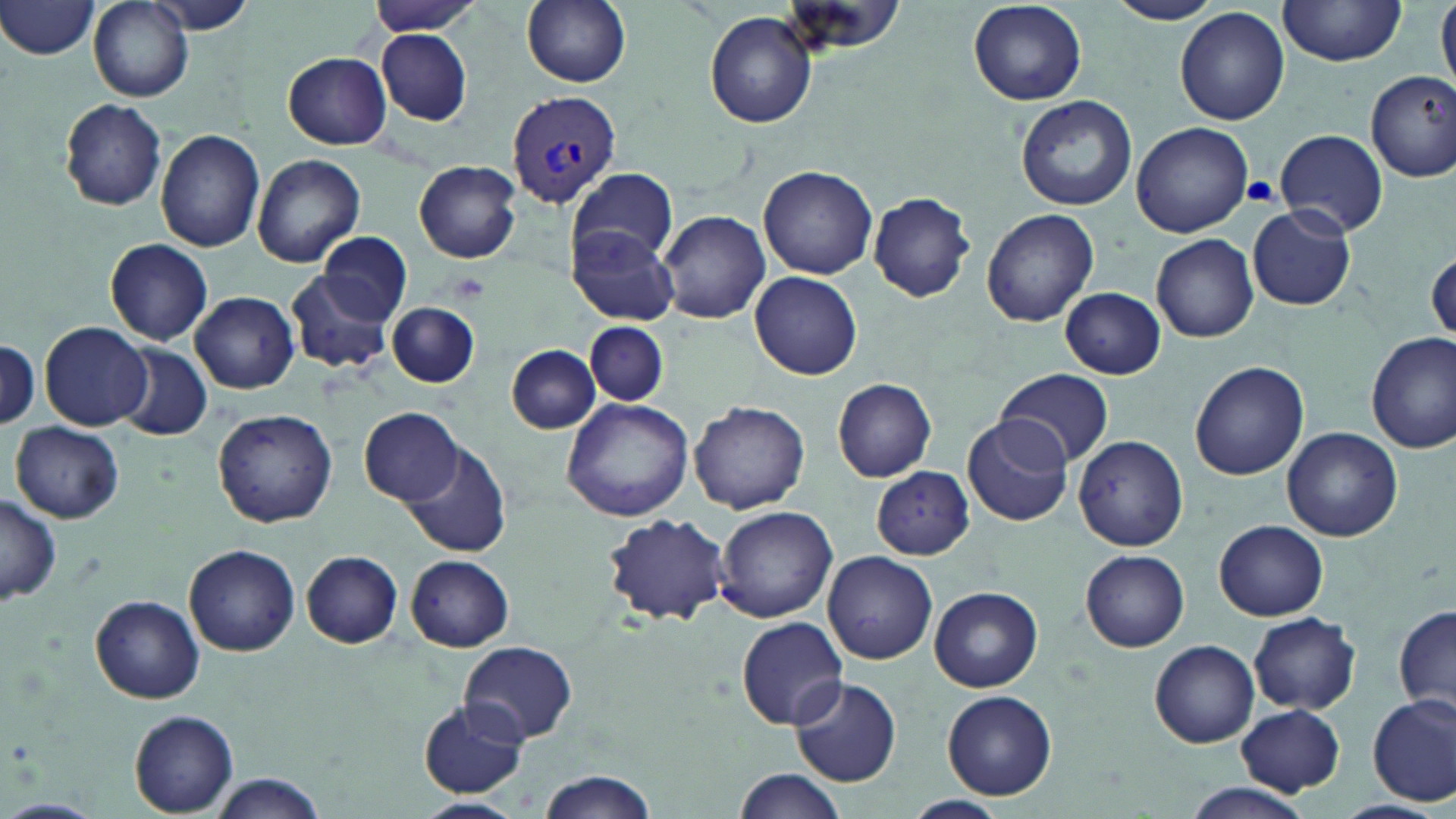

Summary:
  - Coordinate format: approximate bounding boxes as (x1,y1)-(x2,y2) corner pairs in pixels
  - Uninfected red blood cell locations: (0,0)-(101,59), (364,0)-(482,36), (521,0)-(632,87), (1106,0)-(1221,25), (1436,0)-(1456,91), (90,1)-(191,102), (967,1)-(1086,106), (1277,1)-(1408,66), (144,2)-(259,37), (773,2)-(912,61), (1175,7)-(1290,125), (706,12)-(817,128), (376,29)-(472,126), (281,52)-(391,149), (1364,71)-(1455,182), (1016,95)-(1138,211), (59,100)-(168,211), (1132,122)-(1253,237), (155,129)-(265,253), (1273,129)-(1389,237), (253,154)-(366,267), (415,161)-(522,262), (759,165)-(878,280), (568,166)-(678,267), (867,192)-(976,303), (1246,206)-(1356,311), (982,207)-(1100,327), (658,209)-(770,324), (567,226)-(679,326), (318,232)-(411,325), (1152,234)-(1259,343), (104,238)-(214,344), (285,266)-(395,376), (751,271)-(863,380), (1060,287)-(1166,379), (191,292)-(299,393), (388,300)-(481,388), (585,320)-(667,407), (41,321)-(152,430), (1367,332)-(1456,454), (1,338)-(40,431), (113,343)-(213,440), (506,345)-(600,433), (1189,360)-(1309,480), (994,368)-(1114,468), (831,378)-(937,482), (561,396)-(697,522), (689,399)-(812,513), (360,406)-(464,505), (213,408)-(338,529), (962,414)-(1073,527), (11,420)-(125,523), (1283,427)-(1401,540), (1073,435)-(1189,551), (401,440)-(511,558), (871,465)-(974,559), (0,492)-(62,604), (714,505)-(837,623), (600,511)-(732,627), (1216,519)-(1327,620), (185,544)-(301,655), (300,550)-(404,648), (824,550)-(936,664), (1081,551)-(1190,651), (406,555)-(514,651), (931,585)-(1043,692), (91,595)-(204,704), (1395,606)-(1455,717), (1249,612)-(1361,714), (736,616)-(848,729), (459,640)-(577,744), (1149,640)-(1259,748), (789,677)-(903,786), (941,689)-(1058,800), (1368,694)-(1456,807), (420,700)-(529,798), (1236,703)-(1347,794), (129,711)-(239,816), (732,768)-(842,818), (535,769)-(658,819), (206,772)-(329,818), (1185,783)-(1312,819), (903,794)-(1010,819), (409,796)-(524,819), (1332,797)-(1445,819)
  - Plasmodium vivax-infected red blood cell locations: (505,89)-(625,206)
  - Platelet locations: (1241,177)-(1279,207), (450,271)-(489,303)
  - Slide-level diagnosis: Plasmodium vivax
  - Preparation: thin blood film
  - Magnification: 1000x
  - Field of view: single
  - Stain: May-Grünwald-Giemsa
  - Modality: optical microscopy
  - Image size: 1456×819 pixels